Classify this cell by malaria status.
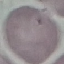
It is uninfected.

Thin smear of blood. Giemsa-stained preparation. Acquired by smartphone through the microscope eyepiece. Automatically extracted cell patch, resized to 64 × 64 pixels.